Evaluate for malaria.
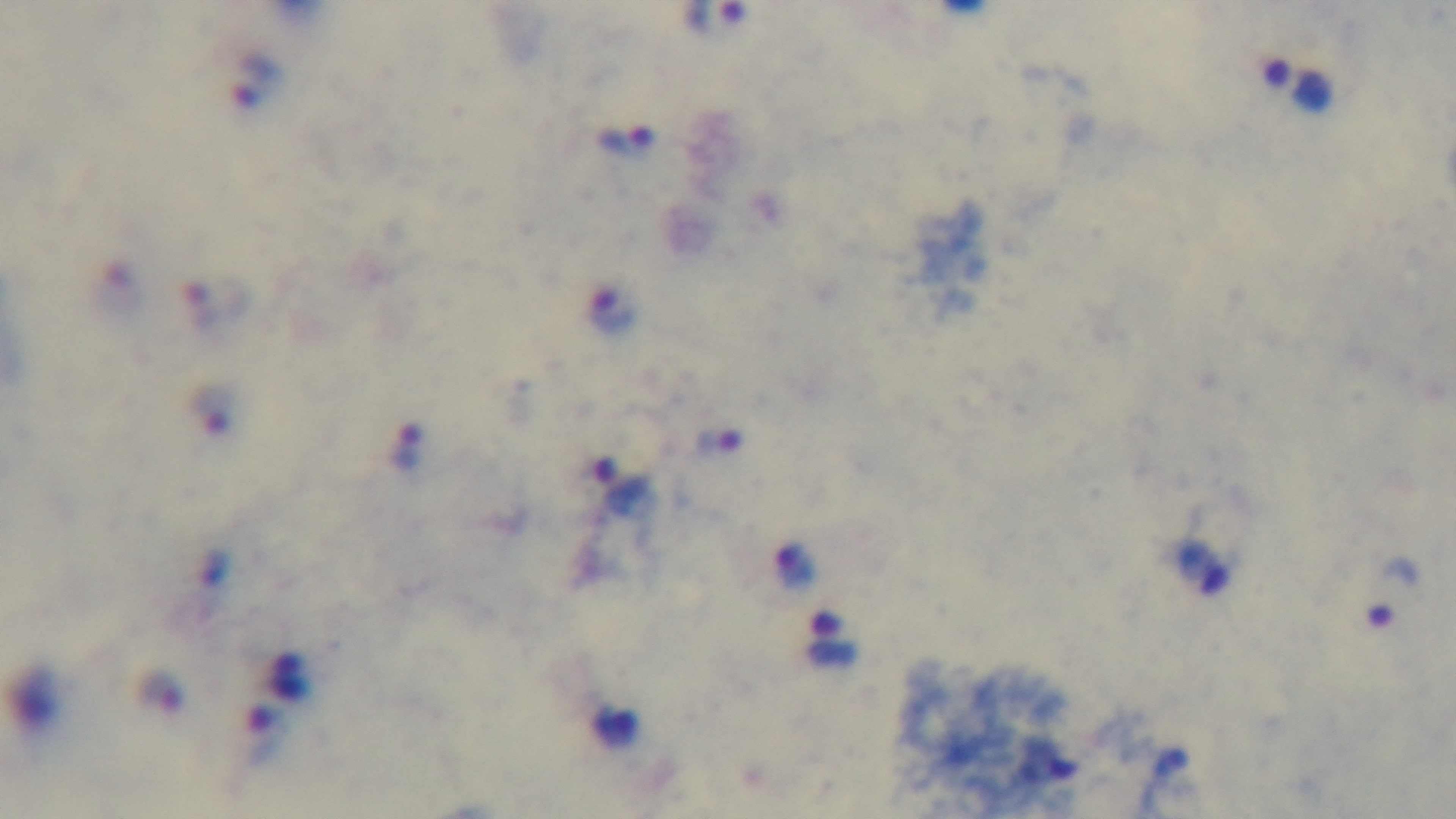
Infected.

stain: Giemsa
capture: mounted 4K digital camera
objective: 100x oil immersion
field_of_view: single
modality: light microscopy
preparation: thick